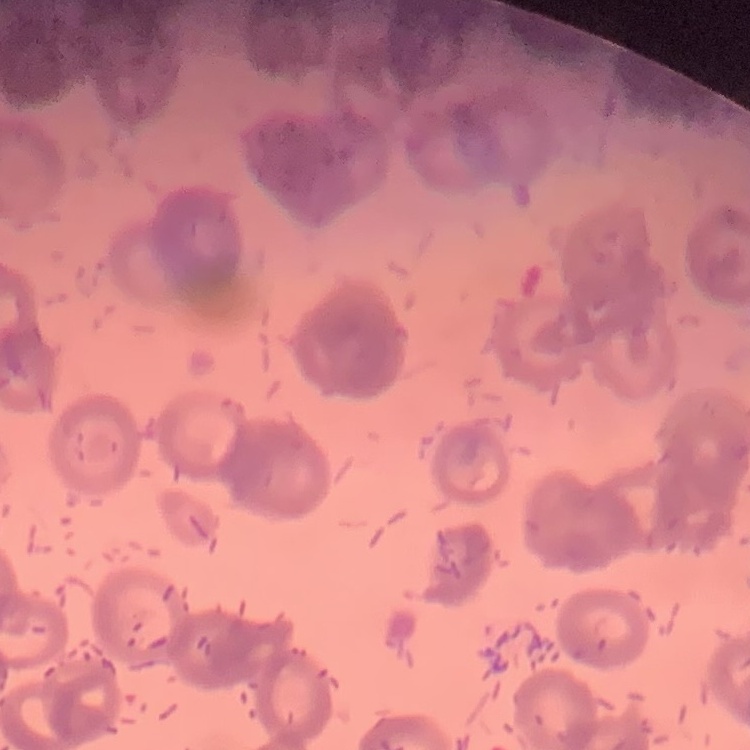

Summary:
  - Red blood cell morphology: rouleaux formation
  - Preparation: thin blood film
  - Stain: Field's or Giemsa
  - Image type: one tile cut from a larger photomicrograph